Give the preparation type.
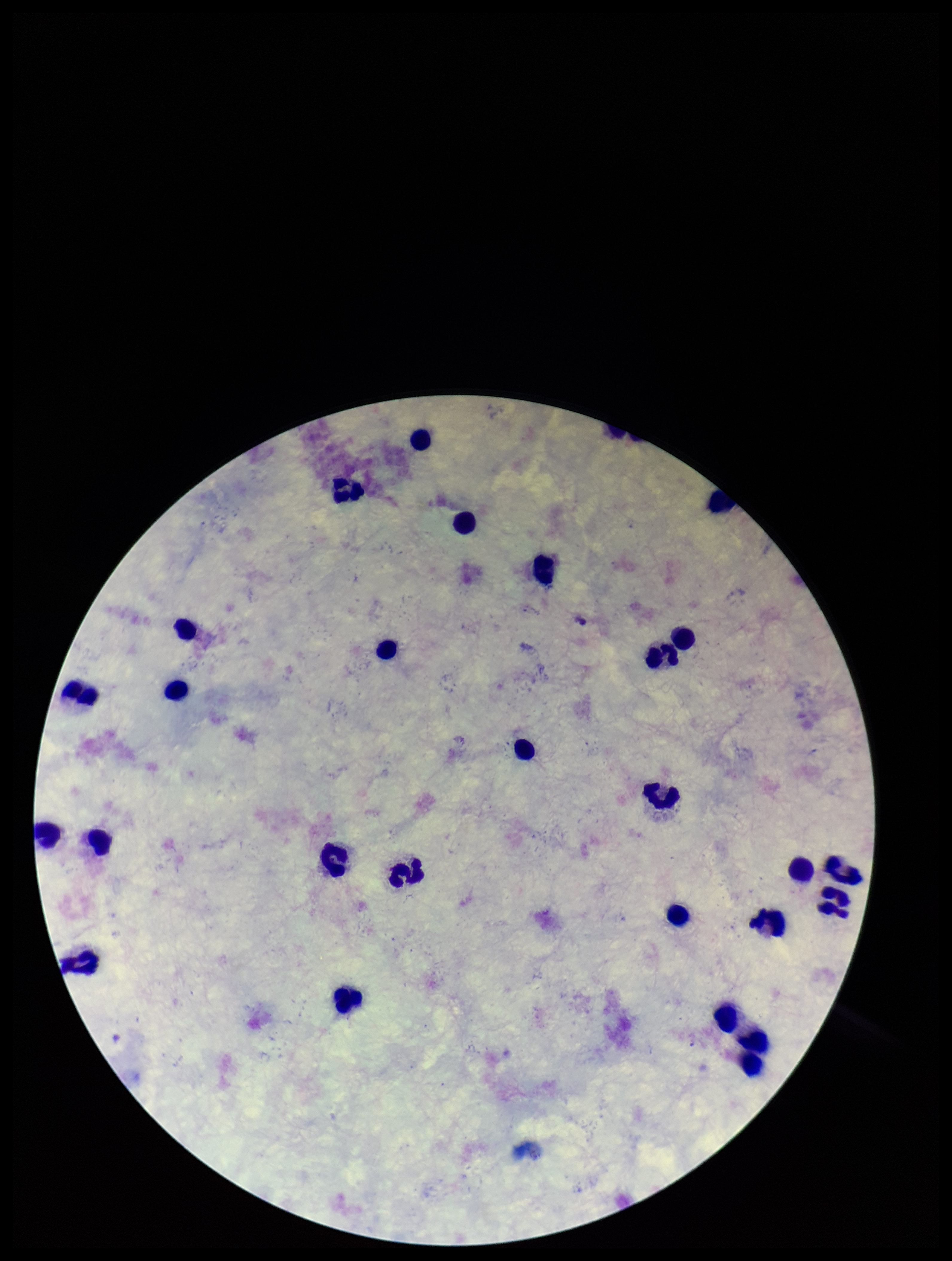

It is a thick blood smear.

One field from this slide. Patient malaria status: negative. Stained with Giemsa. Plasmodium parasites: none identified. Leukocyte count: 26. Parasite count: 0. Photographed through the microscope eyepiece with a smartphone camera. Image is 952×1261 pixels.